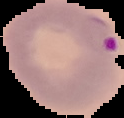 Malaria status: parasitized. The area outside the segmented cell region is set to black. Image is 124×118 pixels. From a thin blood film.